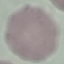
{
  "malaria_status": "uninfected",
  "stain": "Giemsa",
  "preparation": "thin blood film",
  "image_type": "automatically extracted cell patch, resized to 64 × 64 pixels",
  "capture": "smartphone camera at the microscope eyepiece"
}